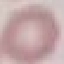

Result: no malaria parasites seen. Giemsa-stained preparation. Photographed with a smartphone camera at the microscope eyepiece. Thin blood film. Automatically extracted cell patch, resized to 64 × 64 pixels.